Outline each Plasmodium malariae-infected red blood cell.
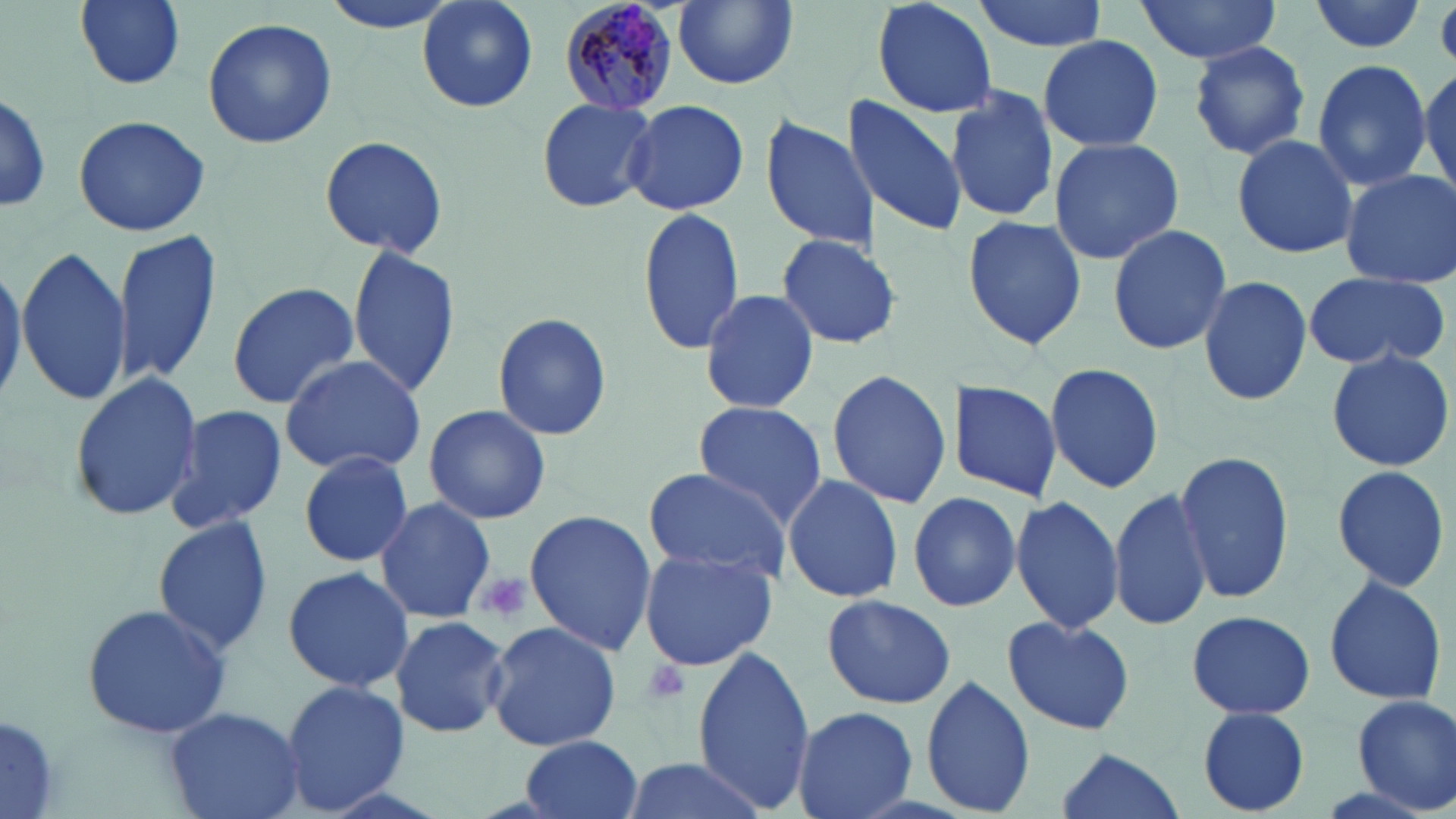

Approximate bounding boxes as named x1/y1/x2/y2 corners in pixels.
Plasmodium malariae-infected red blood cells: (x1=558, y1=0, x2=682, y2=115).

slide-level diagnosis = Plasmodium malariae
preparation = thin blood film
magnification = 1000x
platelet locations = approximate bounding boxes as named x1/y1/x2/y2 corners in pixels: (x1=473, y1=571, x2=533, y2=625), (x1=640, y1=659, x2=693, y2=706)
image size = 1456×819 pixels
uninfected red blood cell locations = approximate bounding boxes as named x1/y1/x2/y2 corners in pixels: (x1=75, y1=0, x2=186, y2=89), (x1=316, y1=0, x2=463, y2=33), (x1=415, y1=0, x2=539, y2=114), (x1=672, y1=0, x2=799, y2=89), (x1=869, y1=0, x2=999, y2=118), (x1=973, y1=0, x2=1107, y2=51), (x1=1132, y1=0, x2=1287, y2=65), (x1=1309, y1=0, x2=1426, y2=54), (x1=202, y1=17, x2=335, y2=150), (x1=1036, y1=34, x2=1165, y2=153), (x1=1186, y1=40, x2=1312, y2=161), (x1=1311, y1=59, x2=1432, y2=193), (x1=1418, y1=61, x2=1455, y2=204), (x1=945, y1=86, x2=1059, y2=222), (x1=0, y1=87, x2=51, y2=214), (x1=843, y1=94, x2=968, y2=237), (x1=536, y1=97, x2=657, y2=212), (x1=623, y1=98, x2=749, y2=216), (x1=758, y1=113, x2=881, y2=254), (x1=73, y1=115, x2=210, y2=237), (x1=319, y1=133, x2=447, y2=260), (x1=1231, y1=133, x2=1359, y2=259), (x1=1049, y1=136, x2=1185, y2=266), (x1=1340, y1=171, x2=1456, y2=286), (x1=638, y1=204, x2=747, y2=356), (x1=960, y1=214, x2=1089, y2=351), (x1=1107, y1=224, x2=1233, y2=356), (x1=113, y1=229, x2=222, y2=388), (x1=774, y1=233, x2=903, y2=350), (x1=16, y1=244, x2=133, y2=406), (x1=348, y1=244, x2=462, y2=401), (x1=1301, y1=270, x2=1451, y2=372), (x1=1198, y1=276, x2=1313, y2=406), (x1=226, y1=281, x2=359, y2=408), (x1=696, y1=289, x2=823, y2=417), (x1=491, y1=311, x2=613, y2=441), (x1=1325, y1=349, x2=1454, y2=472), (x1=278, y1=352, x2=428, y2=478), (x1=1043, y1=361, x2=1166, y2=494), (x1=825, y1=369, x2=953, y2=510), (x1=69, y1=374, x2=203, y2=521), (x1=946, y1=380, x2=1062, y2=500), (x1=692, y1=400, x2=830, y2=529), (x1=164, y1=404, x2=289, y2=536), (x1=423, y1=404, x2=551, y2=526), (x1=1172, y1=448, x2=1294, y2=604), (x1=298, y1=450, x2=412, y2=567), (x1=1332, y1=463, x2=1453, y2=592), (x1=642, y1=467, x2=792, y2=585), (x1=783, y1=472, x2=906, y2=606), (x1=1109, y1=487, x2=1213, y2=631), (x1=907, y1=490, x2=1023, y2=613), (x1=372, y1=497, x2=497, y2=626), (x1=1009, y1=498, x2=1124, y2=635), (x1=523, y1=510, x2=658, y2=657), (x1=152, y1=516, x2=275, y2=656), (x1=638, y1=547, x2=776, y2=671), (x1=282, y1=565, x2=413, y2=693), (x1=1322, y1=572, x2=1449, y2=708), (x1=822, y1=593, x2=955, y2=711), (x1=81, y1=602, x2=233, y2=742), (x1=1187, y1=608, x2=1317, y2=718), (x1=389, y1=614, x2=511, y2=739), (x1=999, y1=615, x2=1135, y2=735), (x1=483, y1=621, x2=622, y2=754), (x1=692, y1=647, x2=815, y2=812), (x1=920, y1=674, x2=1035, y2=814), (x1=279, y1=679, x2=408, y2=813), (x1=1350, y1=694, x2=1456, y2=814), (x1=164, y1=706, x2=305, y2=819), (x1=790, y1=706, x2=917, y2=819), (x1=1196, y1=706, x2=1312, y2=815), (x1=0, y1=707, x2=62, y2=818), (x1=518, y1=734, x2=644, y2=819), (x1=1050, y1=747, x2=1185, y2=819), (x1=619, y1=752, x2=768, y2=819)
stain = May-Grünwald-Giemsa
modality = light microscopy
field of view = single